Outline platelets.
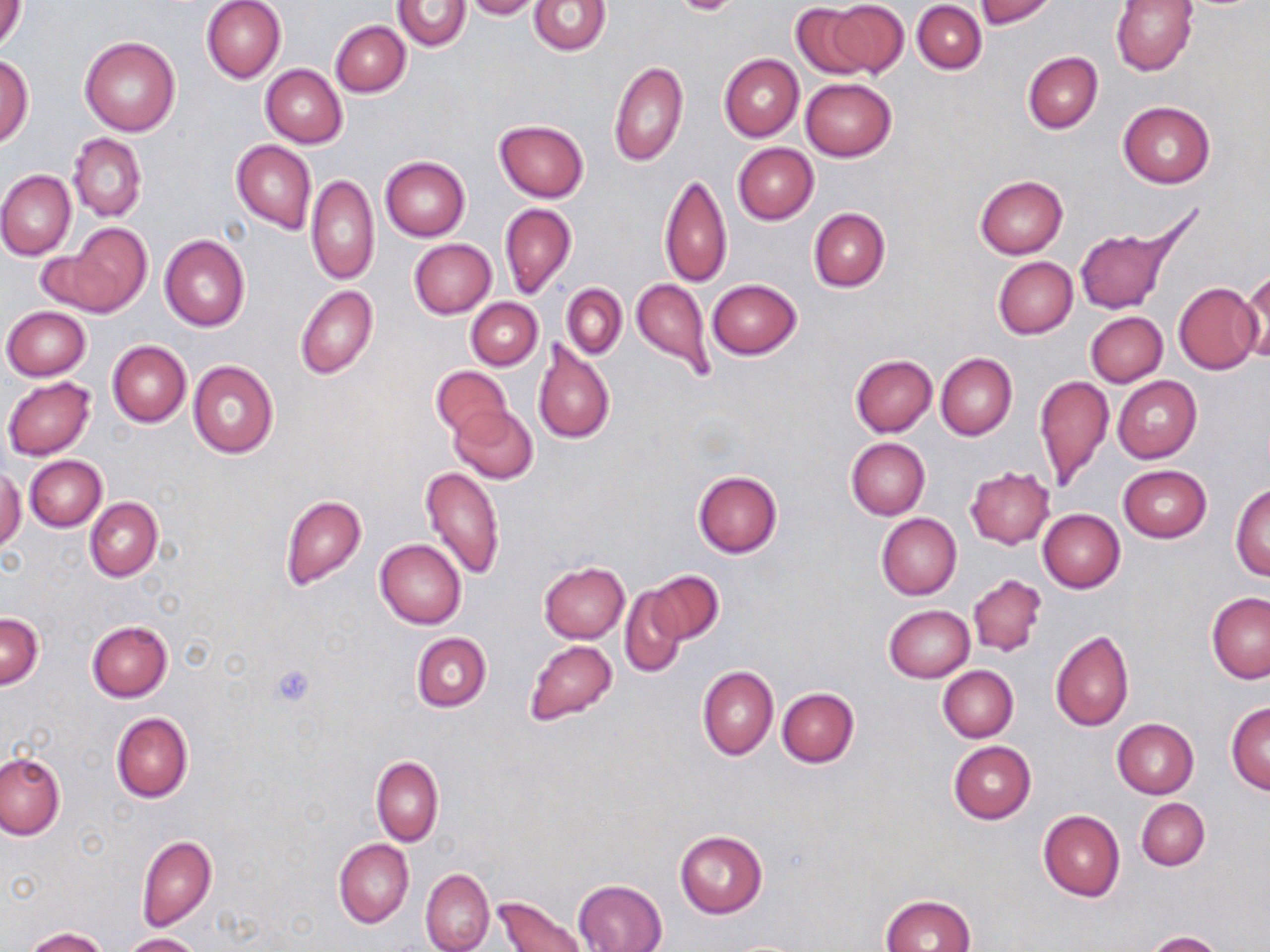
Approximate bounding boxes as (x1, y1, x2, y2) in pixels.
Platelets: (268, 662, 316, 709).

Summary:
  - Uninfected red blood cell locations: (0, 0, 27, 53), (200, 0, 287, 83), (464, 0, 542, 20), (529, 0, 609, 55), (974, 0, 1054, 28), (1111, 0, 1197, 75), (394, 1, 471, 51), (825, 2, 909, 76), (913, 2, 986, 73), (792, 4, 872, 79), (330, 21, 410, 96), (81, 38, 178, 136), (1022, 51, 1103, 134), (0, 53, 33, 148), (719, 53, 803, 142), (608, 61, 689, 167), (261, 65, 347, 148), (800, 78, 897, 161), (1118, 102, 1216, 189), (494, 119, 588, 202), (68, 134, 146, 222), (232, 141, 317, 234), (733, 143, 818, 224), (380, 156, 469, 241), (0, 170, 76, 260), (658, 171, 731, 289), (306, 173, 379, 285), (975, 175, 1068, 258), (499, 203, 576, 300), (808, 208, 890, 292), (1073, 218, 1188, 315), (56, 223, 153, 319), (159, 234, 250, 331), (408, 238, 496, 319), (993, 257, 1078, 339), (1237, 273, 1269, 365), (631, 278, 715, 382), (708, 279, 802, 358), (1173, 282, 1262, 373), (562, 283, 626, 359), (296, 286, 378, 380), (466, 298, 542, 370), (1, 306, 91, 381), (1086, 311, 1168, 386), (532, 338, 615, 445), (107, 340, 190, 428), (936, 352, 1017, 440), (850, 354, 937, 437), (188, 360, 278, 458), (431, 366, 513, 441), (1033, 374, 1113, 490), (3, 376, 96, 459), (1113, 376, 1201, 463), (450, 405, 537, 483), (845, 437, 929, 520), (25, 455, 106, 531), (420, 465, 505, 580), (1118, 465, 1211, 543), (965, 467, 1055, 548), (0, 469, 26, 553), (693, 470, 782, 557), (1230, 483, 1270, 580), (280, 494, 367, 590), (85, 497, 161, 581), (1038, 510, 1125, 592), (876, 513, 961, 599), (375, 539, 467, 629), (539, 562, 629, 642), (651, 570, 723, 644), (967, 573, 1047, 657), (619, 585, 689, 679), (1207, 593, 1270, 684), (884, 605, 975, 682), (1, 613, 43, 689), (87, 621, 172, 702), (1050, 630, 1134, 731), (411, 631, 491, 712), (525, 639, 617, 725), (698, 665, 778, 761), (938, 665, 1018, 742), (777, 687, 859, 767), (1226, 703, 1270, 794), (112, 712, 193, 802), (1111, 719, 1198, 798), (948, 741, 1036, 823), (1, 752, 66, 840), (371, 756, 443, 845), (1137, 798, 1210, 871), (1038, 811, 1125, 901), (674, 829, 768, 918), (137, 836, 217, 932), (334, 839, 414, 928), (420, 868, 494, 952), (574, 879, 668, 952), (495, 894, 585, 952), (880, 894, 976, 951), (23, 928, 108, 951), (1143, 931, 1222, 952), (121, 933, 201, 952)
  - Slide-level diagnosis: negative for blood parasites
  - Preparation: thin blood smear
  - Image size: 1270×952 pixels
  - Modality: light microscopy
  - Stain: May-Grünwald-Giemsa
  - Magnification: 1000x
  - Field of view: one of a larger specimen